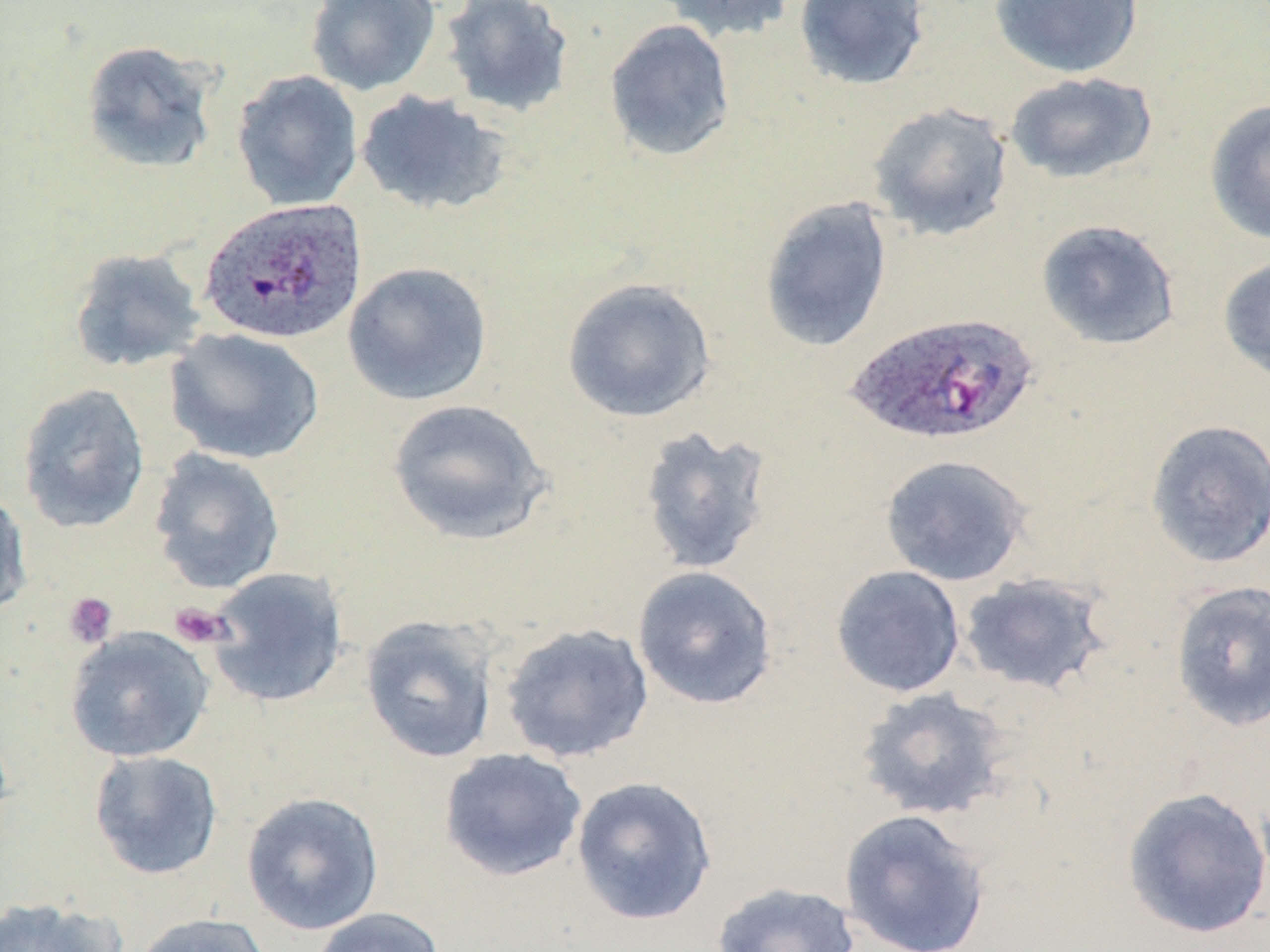

slide-level diagnosis = Plasmodium ovale
magnification = 1000x
modality = light microscopy
preparation = thin blood smear
platelet locations = approximate bounding boxes as named x1/y1/x2/y2 corners in pixels: (x1=63, y1=591, x2=118, y2=648), (x1=169, y1=602, x2=232, y2=649)
Plasmodium ovale-infected red blood cell locations = approximate bounding boxes as named x1/y1/x2/y2 corners in pixels: (x1=198, y1=197, x2=368, y2=346), (x1=844, y1=311, x2=1039, y2=447)
field of view = single
image size = 1270×952 pixels
uninfected red blood cell locations = approximate bounding boxes as named x1/y1/x2/y2 corners in pixels: (x1=304, y1=0, x2=441, y2=97), (x1=439, y1=0, x2=575, y2=119), (x1=656, y1=0, x2=799, y2=44), (x1=793, y1=0, x2=931, y2=91), (x1=988, y1=0, x2=1144, y2=79), (x1=603, y1=18, x2=736, y2=163), (x1=80, y1=40, x2=219, y2=173), (x1=231, y1=69, x2=363, y2=211), (x1=1004, y1=71, x2=1158, y2=184), (x1=354, y1=90, x2=512, y2=216), (x1=1204, y1=98, x2=1270, y2=244), (x1=867, y1=102, x2=1014, y2=241), (x1=759, y1=197, x2=893, y2=353), (x1=1036, y1=219, x2=1181, y2=351), (x1=68, y1=247, x2=206, y2=373), (x1=1218, y1=255, x2=1270, y2=382), (x1=343, y1=261, x2=493, y2=406), (x1=561, y1=277, x2=717, y2=424), (x1=164, y1=326, x2=324, y2=465), (x1=16, y1=382, x2=150, y2=534), (x1=387, y1=398, x2=552, y2=545), (x1=1145, y1=418, x2=1270, y2=568), (x1=637, y1=425, x2=775, y2=576), (x1=149, y1=448, x2=285, y2=594), (x1=880, y1=454, x2=1032, y2=587), (x1=0, y1=489, x2=33, y2=620), (x1=632, y1=565, x2=779, y2=710), (x1=831, y1=565, x2=966, y2=698), (x1=204, y1=566, x2=349, y2=707), (x1=957, y1=572, x2=1112, y2=696), (x1=1169, y1=580, x2=1270, y2=732), (x1=359, y1=615, x2=499, y2=764), (x1=499, y1=622, x2=655, y2=763), (x1=64, y1=626, x2=214, y2=763), (x1=855, y1=687, x2=1011, y2=821), (x1=438, y1=747, x2=587, y2=882), (x1=88, y1=749, x2=224, y2=880), (x1=571, y1=776, x2=717, y2=927), (x1=1122, y1=787, x2=1270, y2=939), (x1=241, y1=791, x2=384, y2=935), (x1=838, y1=808, x2=992, y2=952), (x1=711, y1=881, x2=860, y2=952), (x1=0, y1=895, x2=125, y2=952), (x1=309, y1=907, x2=445, y2=952), (x1=130, y1=912, x2=272, y2=952)
stain = May-Grünwald-Giemsa